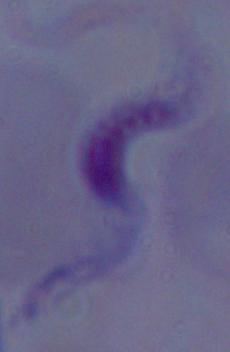

identification = trypanosome
modality = micrograph
magnification = 1000x